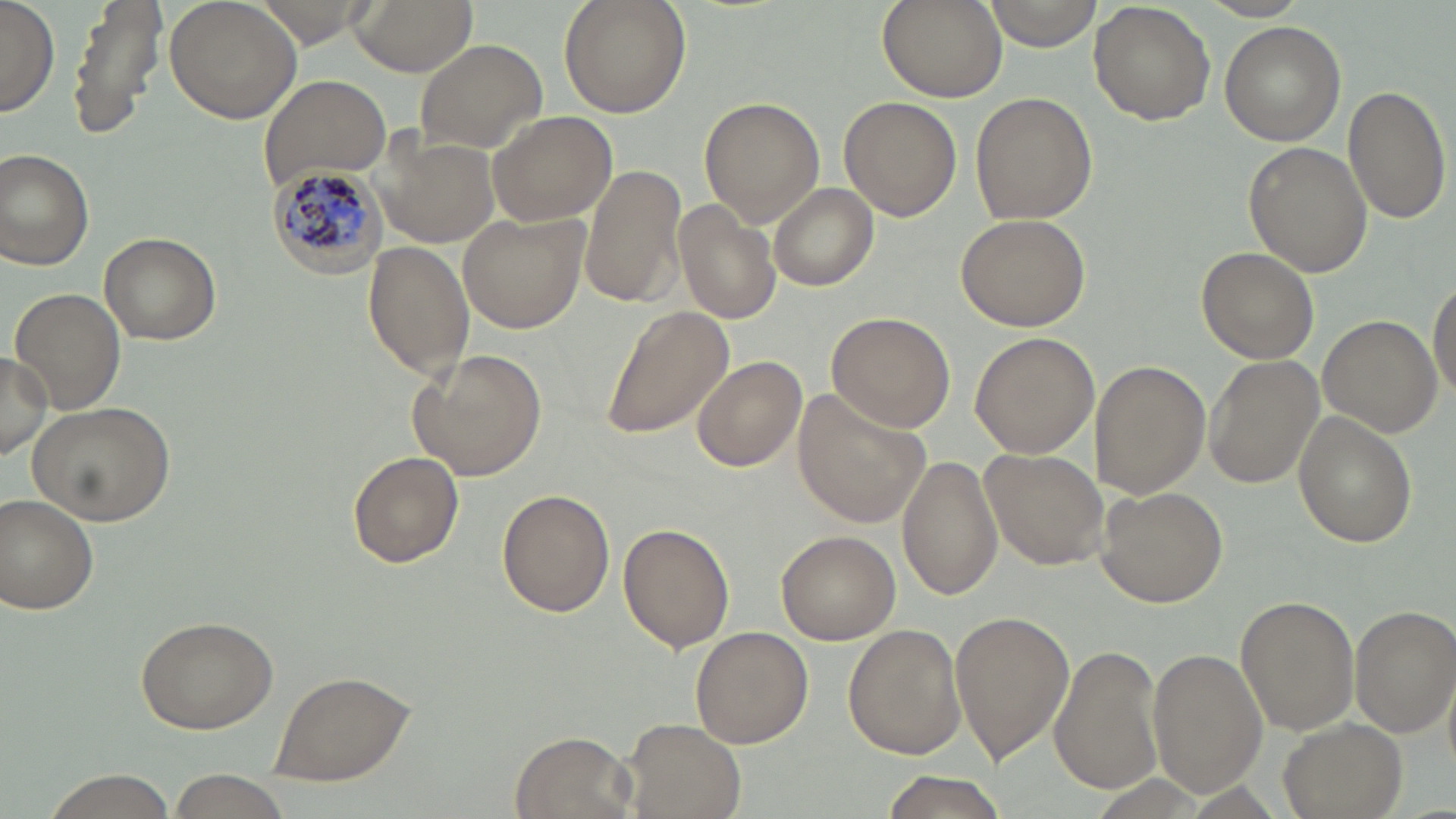
Plasmodium malariae-infected red blood cell locations = approximate bounding boxes as (x1,y1)-(x2,y2) corner pairs in pixels: (264,163)-(386,275)
slide-level diagnosis = Plasmodium malariae
stain = May-Grünwald-Giemsa
preparation = thin blood smear
magnification = 1000x
field of view = single
uninfected red blood cell locations = approximate bounding boxes as (x1,y1)-(x2,y2) corner pairs in pixels: (66,0)-(168,138), (163,0)-(301,124), (346,0)-(479,74), (558,0)-(692,118), (877,0)-(1006,102), (981,0)-(1099,51), (0,2)-(58,115), (1089,2)-(1216,125), (1220,21)-(1346,145), (414,38)-(549,156), (258,74)-(390,187), (1342,85)-(1450,223), (972,92)-(1096,227), (840,96)-(962,222), (699,98)-(824,226), (485,109)-(618,226), (376,133)-(500,249), (1244,141)-(1373,276), (0,148)-(97,272), (580,166)-(688,310), (769,182)-(879,291), (673,198)-(781,328), (458,213)-(588,333), (956,213)-(1092,332), (100,232)-(220,346), (364,240)-(473,381), (1197,247)-(1318,364), (1429,277)-(1456,401), (11,288)-(125,413), (598,305)-(734,441), (826,311)-(955,434), (1318,316)-(1442,437), (970,332)-(1099,460), (408,349)-(548,480), (0,350)-(50,461), (1205,355)-(1321,488), (693,356)-(807,471), (1091,364)-(1209,498), (794,391)-(933,527), (27,400)-(175,527), (1294,410)-(1418,547), (982,449)-(1107,570), (897,451)-(1003,601), (349,452)-(463,567), (1096,486)-(1227,607), (497,488)-(615,616), (2,494)-(100,614), (619,522)-(735,653), (776,529)-(900,644), (1235,595)-(1359,734), (1350,604)-(1456,739), (950,610)-(1074,764), (135,613)-(280,734), (843,624)-(966,760), (691,627)-(811,747), (1049,644)-(1164,797), (1149,646)-(1267,794), (267,668)-(418,787), (1278,718)-(1405,818), (619,721)-(743,817), (511,731)-(633,818), (39,770)-(179,818), (166,772)-(295,819), (872,774)-(1012,819)
image size = 1456×819 pixels
modality = optical microscopy